Classify this cell by malaria status.
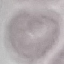
It is uninfected.

Summary:
  - Capture: smartphone through the microscope eyepiece
  - Stain: Giemsa
  - Image type: cell patch, automatically extracted from a larger field of view and resized to 64 × 64 pixels
  - Preparation: thin blood film